Outline each Plasmodium falciparum-infected red blood cell.
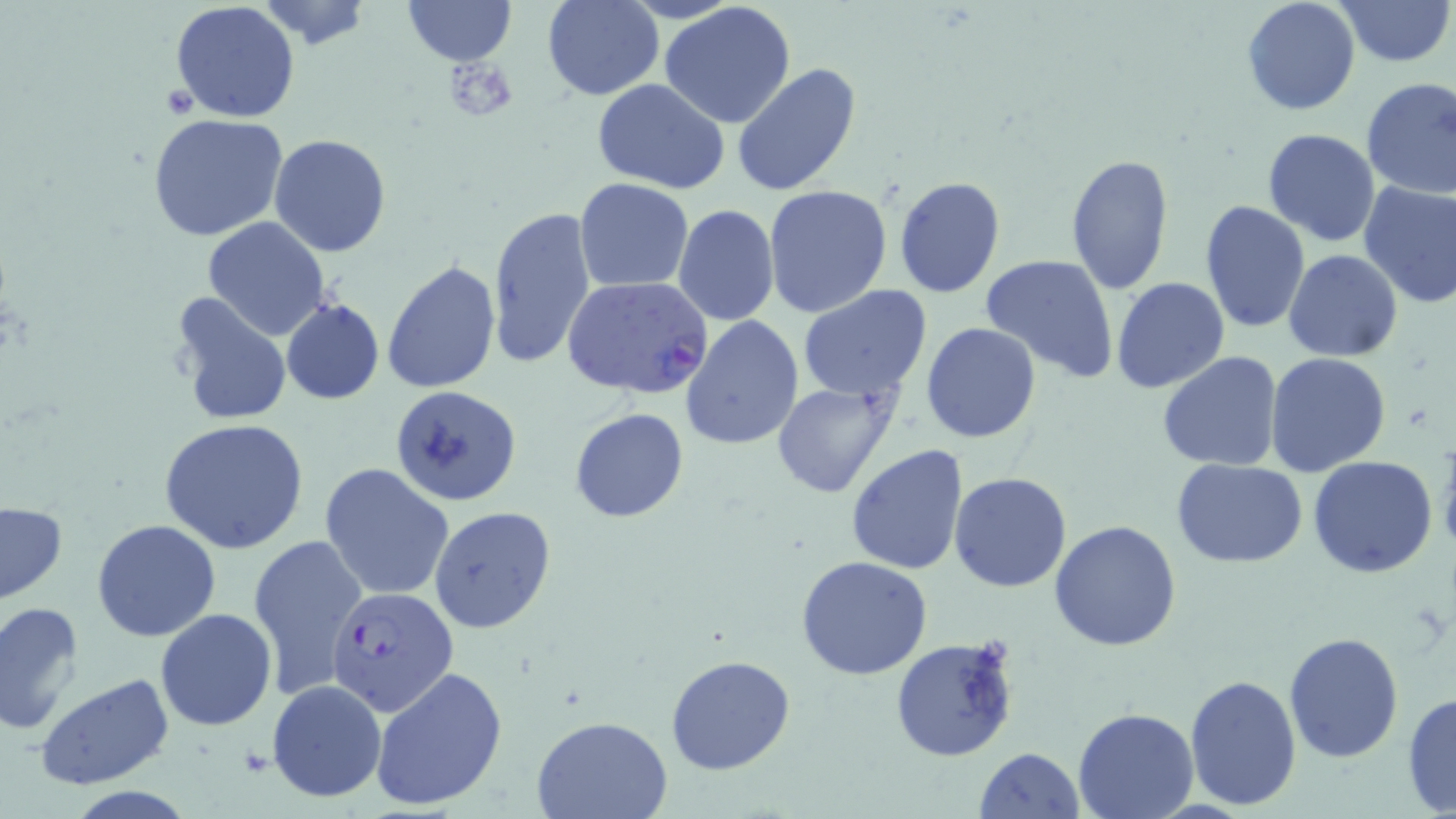
Approximate bounding boxes as [x1, y1, x2, y2] in pixels.
Plasmodium falciparum-infected red blood cells: [561, 275, 714, 400], [327, 590, 457, 721].

Summary:
  - Platelet locations: [449, 63, 515, 120], [157, 85, 199, 119]
  - Uninfected red blood cell locations: [252, 0, 374, 49], [404, 0, 514, 66], [1242, 0, 1360, 116], [1334, 0, 1453, 68], [170, 1, 300, 124], [542, 1, 665, 100], [659, 2, 797, 129], [732, 62, 861, 197], [1360, 77, 1456, 202], [591, 79, 732, 198], [147, 113, 291, 244], [1261, 128, 1380, 246], [269, 134, 393, 257], [1065, 152, 1173, 293], [894, 175, 1006, 299], [574, 178, 694, 292], [1357, 180, 1456, 309], [602, 182, 775, 300], [762, 184, 892, 318], [1200, 200, 1310, 333], [486, 206, 598, 370], [673, 206, 780, 326], [201, 217, 330, 340], [1284, 250, 1402, 363], [979, 253, 1120, 383], [382, 259, 501, 394], [1111, 277, 1230, 394], [798, 285, 932, 402], [170, 293, 293, 427], [281, 298, 383, 403], [681, 313, 803, 453], [921, 323, 1040, 443], [1157, 350, 1283, 471], [1265, 352, 1394, 478], [770, 378, 903, 500], [390, 385, 523, 507], [570, 407, 689, 524], [158, 418, 308, 555], [1438, 433, 1456, 563], [845, 444, 967, 578], [1308, 455, 1439, 578], [1171, 458, 1309, 568], [320, 462, 454, 602], [950, 472, 1072, 592], [0, 501, 67, 605], [429, 506, 555, 634], [92, 519, 220, 641], [1051, 519, 1182, 652], [247, 533, 367, 700], [796, 555, 935, 679], [0, 600, 85, 735], [155, 608, 277, 731], [1282, 630, 1403, 763], [889, 636, 1021, 762], [665, 654, 796, 775], [370, 667, 506, 810], [36, 674, 172, 790], [1184, 675, 1301, 811], [267, 679, 385, 805], [1402, 689, 1456, 819], [1073, 705, 1199, 819], [533, 716, 673, 819], [975, 746, 1085, 818]
  - Slide-level diagnosis: Plasmodium falciparum
  - Modality: light microscopy
  - Stain: May-Grünwald-Giemsa
  - Magnification: 1000x
  - Image size: 1456×819 pixels
  - Field of view: single
  - Preparation: thin blood smear